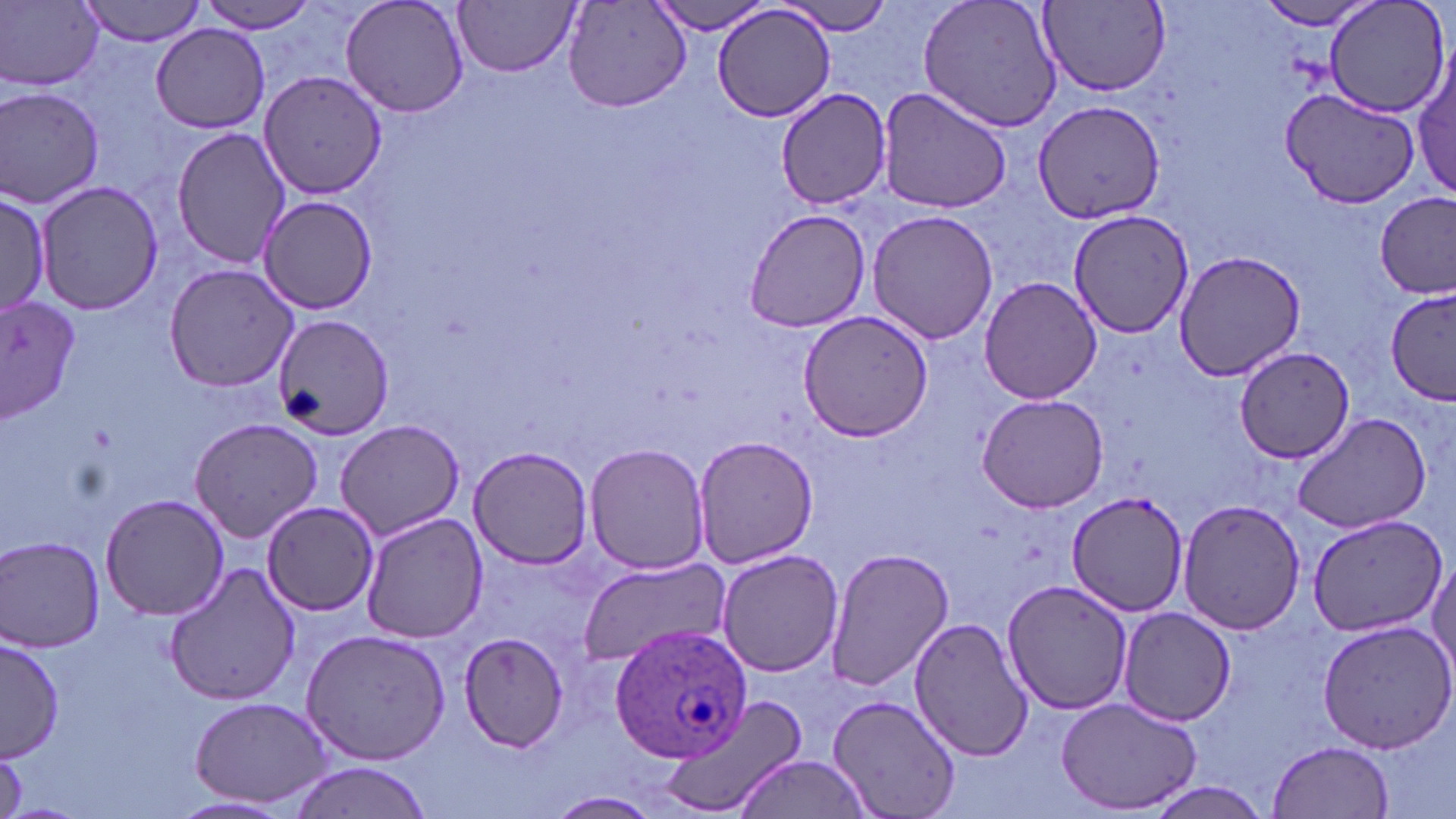
{
  "slide_level_diagnosis": "Plasmodium ovale",
  "stain": "May-Grünwald-Giemsa",
  "preparation": "thin blood smear",
  "modality": "optical microscopy",
  "magnification": "1000x",
  "uninfected_red_blood_cell_locations": "approximate bounding boxes as [x1, y1, x2, y2] in pixels: [77, 0, 212, 46], [197, 0, 321, 32], [339, 0, 471, 120], [649, 0, 777, 36], [918, 0, 1066, 132], [1323, 0, 1450, 118], [3, 1, 104, 91], [456, 1, 580, 77], [1039, 1, 1171, 94], [1255, 1, 1384, 30], [778, 2, 896, 38], [564, 3, 688, 111], [712, 5, 838, 124], [151, 24, 269, 133], [1412, 56, 1456, 200], [256, 68, 390, 199], [2, 85, 107, 209], [875, 86, 1016, 213], [775, 89, 892, 208], [1284, 91, 1424, 207], [1032, 100, 1168, 224], [172, 126, 292, 269], [36, 178, 163, 315], [1375, 190, 1455, 298], [0, 194, 50, 314], [255, 195, 380, 317], [742, 207, 872, 333], [866, 209, 998, 345], [1067, 209, 1195, 338], [1173, 250, 1306, 379], [164, 263, 300, 391], [981, 278, 1101, 404], [1385, 289, 1456, 404], [0, 293, 79, 425], [797, 309, 932, 443], [272, 317, 394, 440], [1236, 346, 1354, 466], [976, 393, 1109, 514], [1290, 410, 1431, 535], [187, 416, 325, 541], [333, 418, 465, 539], [692, 432, 819, 571], [585, 442, 710, 574], [467, 446, 596, 569], [100, 492, 228, 622], [1066, 494, 1188, 621], [1176, 497, 1307, 635], [259, 500, 379, 618], [360, 510, 487, 644], [1305, 515, 1445, 638], [1, 535, 106, 651], [823, 547, 954, 693], [715, 548, 845, 677], [1428, 551, 1456, 683], [575, 556, 732, 666], [162, 561, 301, 708], [1000, 580, 1134, 716], [1117, 606, 1237, 726], [909, 616, 1034, 761], [1316, 621, 1456, 755], [300, 629, 451, 765], [457, 633, 572, 754], [1, 637, 63, 762], [657, 693, 811, 819], [829, 693, 962, 819], [190, 696, 335, 809], [1056, 698, 1201, 815], [1269, 739, 1395, 817], [734, 756, 877, 818], [284, 762, 434, 819], [1146, 783, 1275, 817], [545, 791, 663, 819], [167, 795, 297, 819]",
  "plasmodium_ovale_infected_red_blood_cell_locations": "approximate bounding boxes as [x1, y1, x2, y2] in pixels: [608, 624, 757, 763]",
  "image_size": "1456×819 pixels",
  "field_of_view": "single"
}